Report the malaria status of this cell.
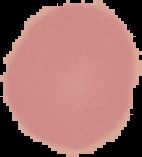

Uninfected.

image type = cell region segmented out of the field of view; surrounding area masked to black
image size = 142×157 pixels
preparation = thin blood smear